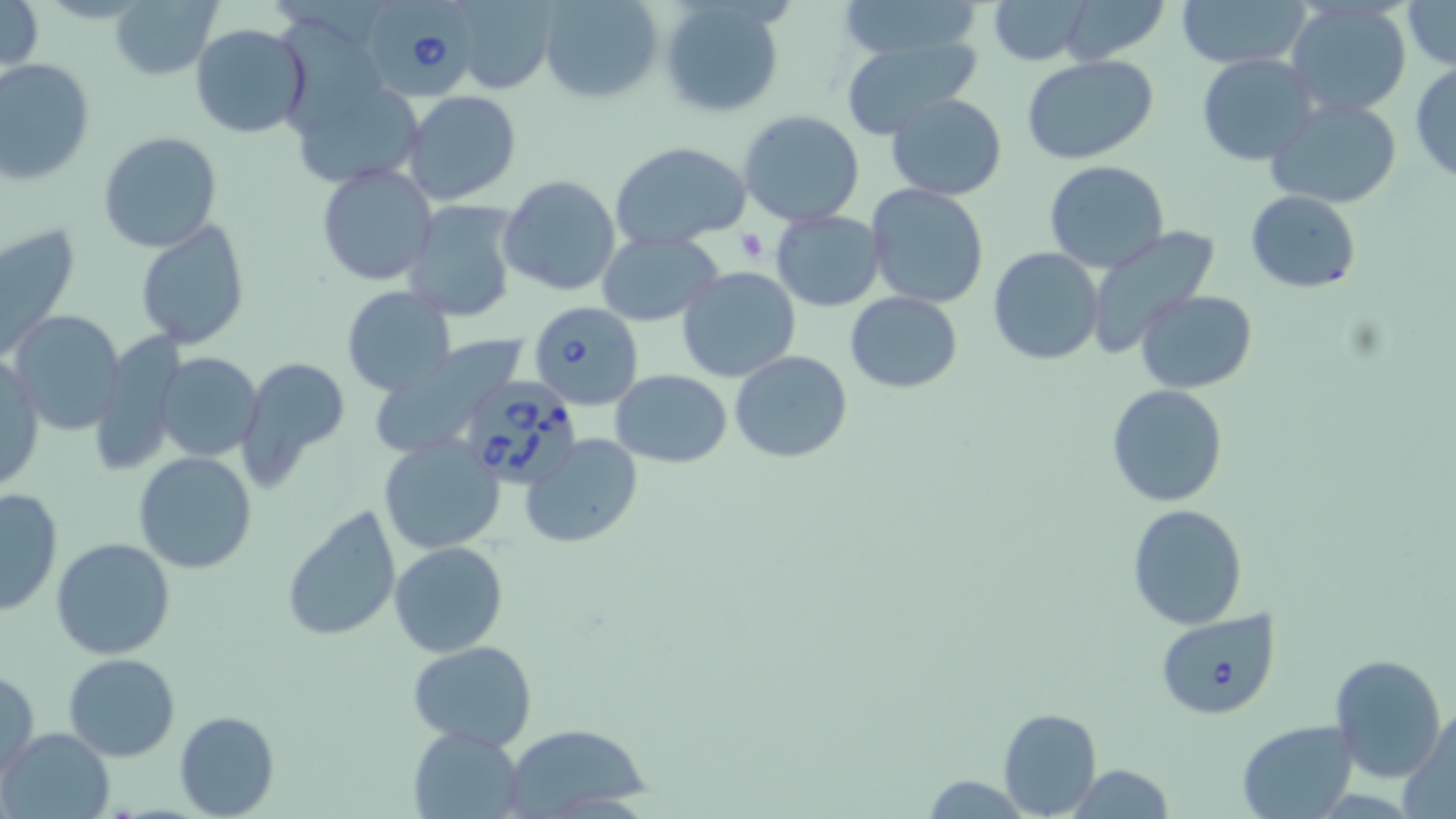
Approximate bounding boxes as [x1, y1, x2, y2] in pixels. Uninfected red blood cell locations: [0, 0, 41, 73], [111, 0, 223, 80], [539, 0, 662, 102], [658, 0, 786, 116], [986, 0, 1091, 64], [1056, 0, 1166, 64], [1180, 0, 1309, 69], [1402, 0, 1456, 70], [832, 2, 991, 60], [449, 3, 559, 95], [1286, 3, 1411, 116], [189, 23, 310, 140], [837, 39, 982, 142], [1198, 53, 1319, 166], [1022, 56, 1160, 166], [1, 58, 95, 185], [1410, 63, 1456, 185], [292, 80, 424, 190], [403, 90, 521, 205], [886, 92, 1007, 201], [1266, 96, 1404, 208], [737, 110, 866, 227], [98, 130, 223, 253], [609, 140, 752, 252], [1044, 160, 1168, 273], [316, 163, 436, 285], [499, 174, 620, 296], [1062, 178, 1190, 322], [866, 183, 988, 309], [1245, 191, 1362, 293], [402, 200, 520, 322], [770, 210, 885, 311], [135, 218, 249, 352], [1, 221, 79, 360], [1086, 226, 1220, 363], [596, 230, 724, 327], [988, 247, 1104, 366], [677, 266, 802, 382], [342, 287, 456, 396], [1135, 289, 1258, 394], [844, 292, 962, 393], [10, 312, 124, 436], [368, 339, 527, 457], [1, 351, 43, 492], [730, 351, 853, 462], [154, 352, 264, 461], [236, 356, 353, 483], [611, 369, 732, 468], [1105, 383, 1228, 508], [520, 434, 640, 548], [379, 436, 507, 555], [135, 451, 256, 574], [0, 488, 62, 614], [1126, 503, 1249, 631], [282, 506, 402, 643], [50, 537, 176, 660], [390, 541, 508, 656], [407, 641, 536, 749], [64, 652, 180, 761], [1331, 652, 1447, 781], [1, 668, 39, 777], [1401, 706, 1455, 816], [997, 707, 1102, 817], [174, 709, 280, 818], [1235, 719, 1357, 818], [500, 725, 647, 815], [3, 727, 115, 818], [407, 727, 526, 818], [1063, 763, 1178, 818], [919, 775, 1029, 816]. Babesia divergens-infected red blood cell locations: [365, 1, 473, 96], [528, 300, 643, 411], [465, 379, 590, 494], [1156, 609, 1281, 719]. Platelet locations: [735, 228, 765, 263]. Slide-level diagnosis: Babesia divergens. May-Grünwald-Giemsa stain. Image is 1456×819 pixels. Thin blood film. Light microscopy. Captured at 1000x magnification. One field of a larger specimen.